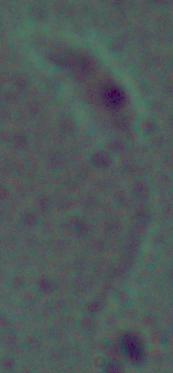

Summary:
  - Identification: Leishmania
  - Magnification: 1000x
  - Modality: micrograph